Locate every malaria parasite.
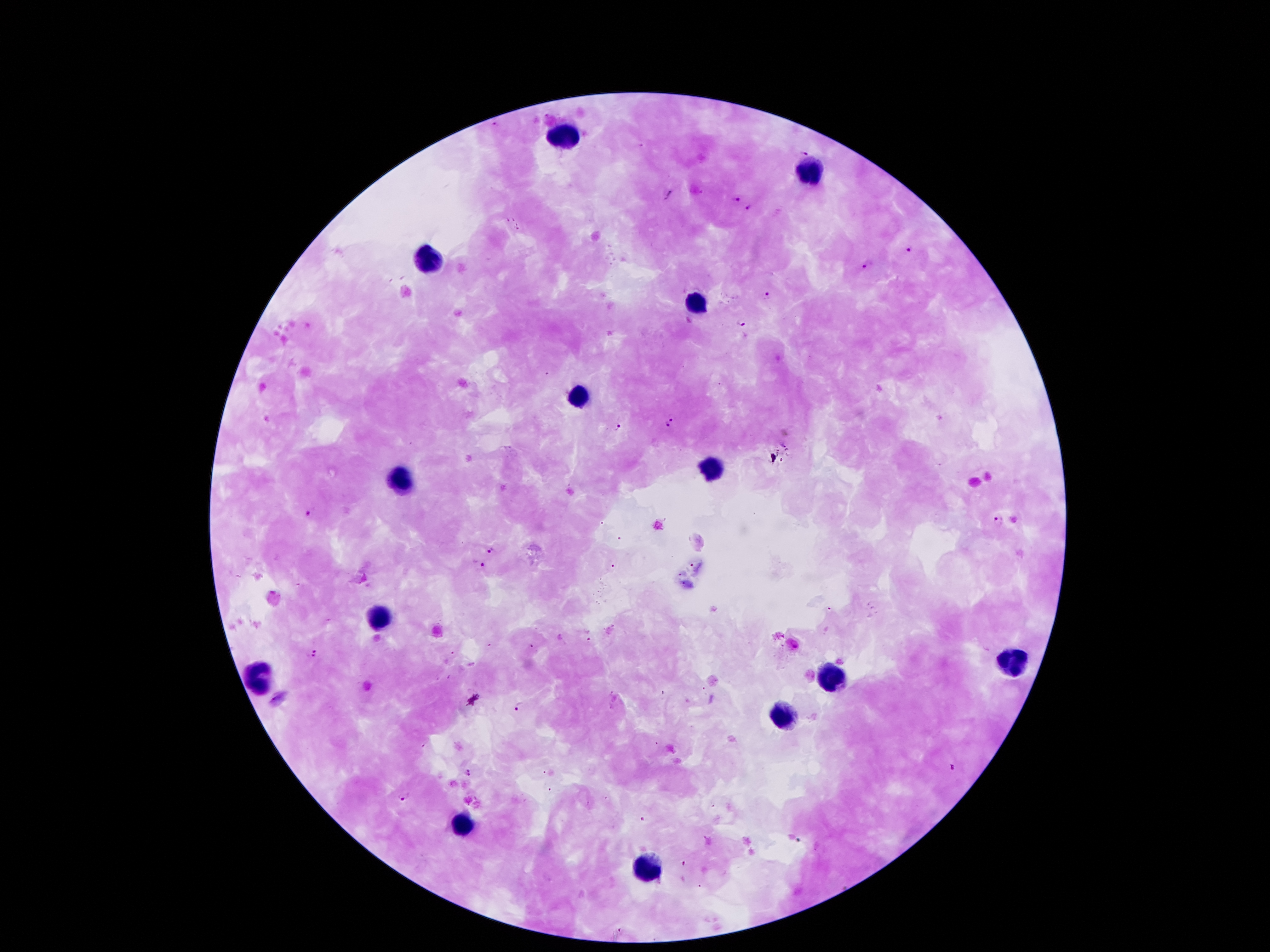
Approximate centers as {x, y} in pixels.
Malaria parasites: {495, 124}, {806, 149}, {668, 194}, {737, 198}, {748, 210}, {910, 249}, {868, 265}, {769, 297}, {743, 324}, {672, 422}, {617, 428}, {310, 511}, {999, 520}, {491, 549}, {480, 565}, {313, 652}, {519, 705}, {466, 772}, {952, 772}, {404, 794}, {798, 839}.

Leukocyte locations: {564, 133}, {809, 171}, {429, 259}, {696, 308}, {577, 398}, {712, 471}, {402, 478}, {382, 617}, {1012, 661}, {265, 675}, {831, 677}, {787, 714}, {460, 825}, {648, 871}. 100x magnification. Photographed through the microscope eyepiece with a smartphone camera. Thick peripheral-blood smear. Image is 1270×952 pixels. Patient malaria status: infected with Plasmodium falciparum. One field from this slide. Giemsa-stained preparation.